Assess this cell for malaria.
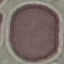

It is uninfected.

{
  "image_type": "automatically extracted cell patch, resized to 64 × 64 pixels",
  "preparation": "thin blood smear",
  "stain": "Giemsa",
  "capture": "smartphone through the microscope eyepiece"
}